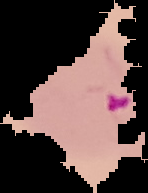

Summary:
  - Image type: segmented cell region on a black background
  - Preparation: thin blood smear
  - Image size: 148×193 pixels
  - Result: Plasmodium parasites detected